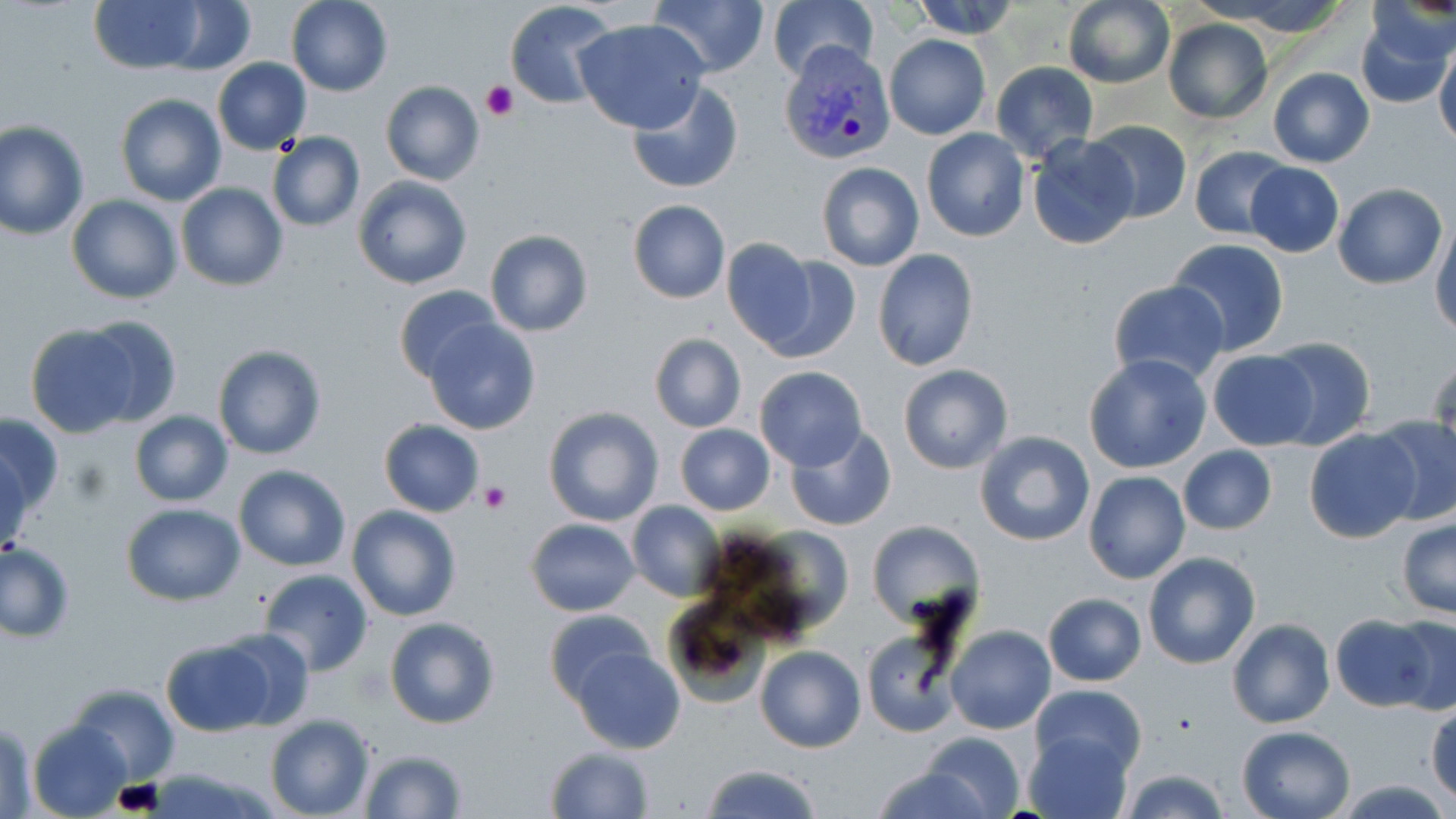

slide_level_diagnosis: Plasmodium vivax
stain: May-Grünwald-Giemsa
image_size: 1456×819 pixels
preparation: thin blood smear
magnification: 1000x
uninfected_red_blood_cell_locations: 'approximate bounding boxes as (x1,y1)-(x2,y2) corner pairs in pixels: (90,0)-(204,73), (285,0)-(394,96), (505,0)-(621,109), (647,0)-(768,77), (767,0)-(878,83), (909,0)-(1022,40), (1061,0)-(1176,89), (162,2)-(255,74), (1355,6)-(1454,111), (1162,18)-(1272,124), (575,20)-(711,135), (884,34)-(990,139), (1433,38)-(1456,150), (212,57)-(312,155), (990,61)-(1096,162), (1268,67)-(1375,167), (380,81)-(484,185), (625,81)-(745,195), (115,93)-(226,206), (0,120)-(90,240), (1086,120)-(1191,225), (921,129)-(1029,242), (266,132)-(366,232), (1027,134)-(1139,251), (1187,145)-(1292,240), (1244,160)-(1344,257), (816,162)-(924,271), (352,175)-(473,291), (176,183)-(287,290), (1332,183)-(1447,288), (66,194)-(182,305), (627,200)-(731,303), (1430,218)-(1456,338), (484,229)-(593,337), (719,238)-(819,352), (1166,238)-(1290,356), (872,248)-(979,371), (758,255)-(860,364), (1108,279)-(1230,384), (392,284)-(503,385), (80,316)-(185,425), (422,317)-(542,436), (23,321)-(145,437), (648,333)-(746,434), (1265,336)-(1376,450), (213,345)-(326,460), (1205,349)-(1319,451), (1428,353)-(1456,461), (1084,354)-(1212,474), (897,364)-(1013,473), (755,366)-(867,469), (543,406)-(663,526), (2,411)-(63,519), (129,411)-(233,507), (1369,415)-(1456,523), (378,419)-(486,517), (675,425)-(776,516), (785,425)-(897,530), (1304,427)-(1419,542), (974,431)-(1095,548), (1176,443)-(1277,535), (1,449)-(29,561), (233,464)-(351,571), (1083,471)-(1189,584), (626,500)-(726,602), (121,503)-(246,605), (347,504)-(461,621), (1397,517)-(1456,620), (525,518)-(641,617), (865,519)-(982,624), (0,541)-(76,642), (1142,552)-(1260,669), (257,569)-(374,677), (1043,593)-(1146,687), (662,598)-(770,709), (545,608)-(655,708), (1329,614)-(1437,711), (1389,615)-(1456,718), (385,616)-(500,730), (1227,618)-(1334,729), (947,625)-(1056,734), (218,628)-(314,730), (861,629)-(962,739), (161,640)-(274,736), (755,645)-(866,753), (571,648)-(685,754), (67,684)-(181,783), (1030,684)-(1146,774), (1426,702)-(1456,803), (263,713)-(375,819), (2,719)-(39,816), (29,721)-(130,816), (1237,726)-(1355,819), (919,731)-(1028,819), (1024,731)-(1133,819), (544,746)-(654,819), (359,747)-(468,818), (870,762)-(995,819), (701,765)-(822,819), (1119,766)-(1232,819), (144,767)-(278,818)'
platelet_locations: 'approximate bounding boxes as (x1,y1)-(x2,y2) corner pairs in pixels: (481,80)-(517,121), (477,480)-(512,513)'
modality: optical microscopy
plasmodium_vivax_infected_red_blood_cell_locations: 'approximate bounding boxes as (x1,y1)-(x2,y2) corner pairs in pixels: (778,42)-(897,165)'
field_of_view: single